Assess the morphology of the erythrocytes.
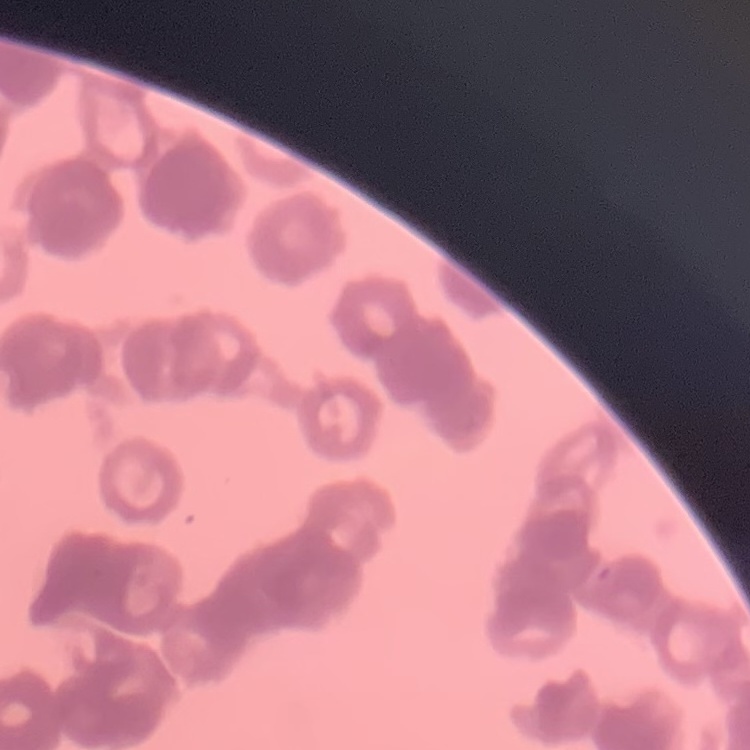

Rouleaux formation.

stain: Field's or Giemsa
preparation: thin peripheral smear
image_type: one tile cut from a larger photomicrograph